Report the malaria status of this cell.
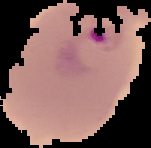

It is parasitized.

image_type: segmented cell region with the area outside set to black
image_size: 151×148 pixels
preparation: thin blood film